Name the blood parasite species.
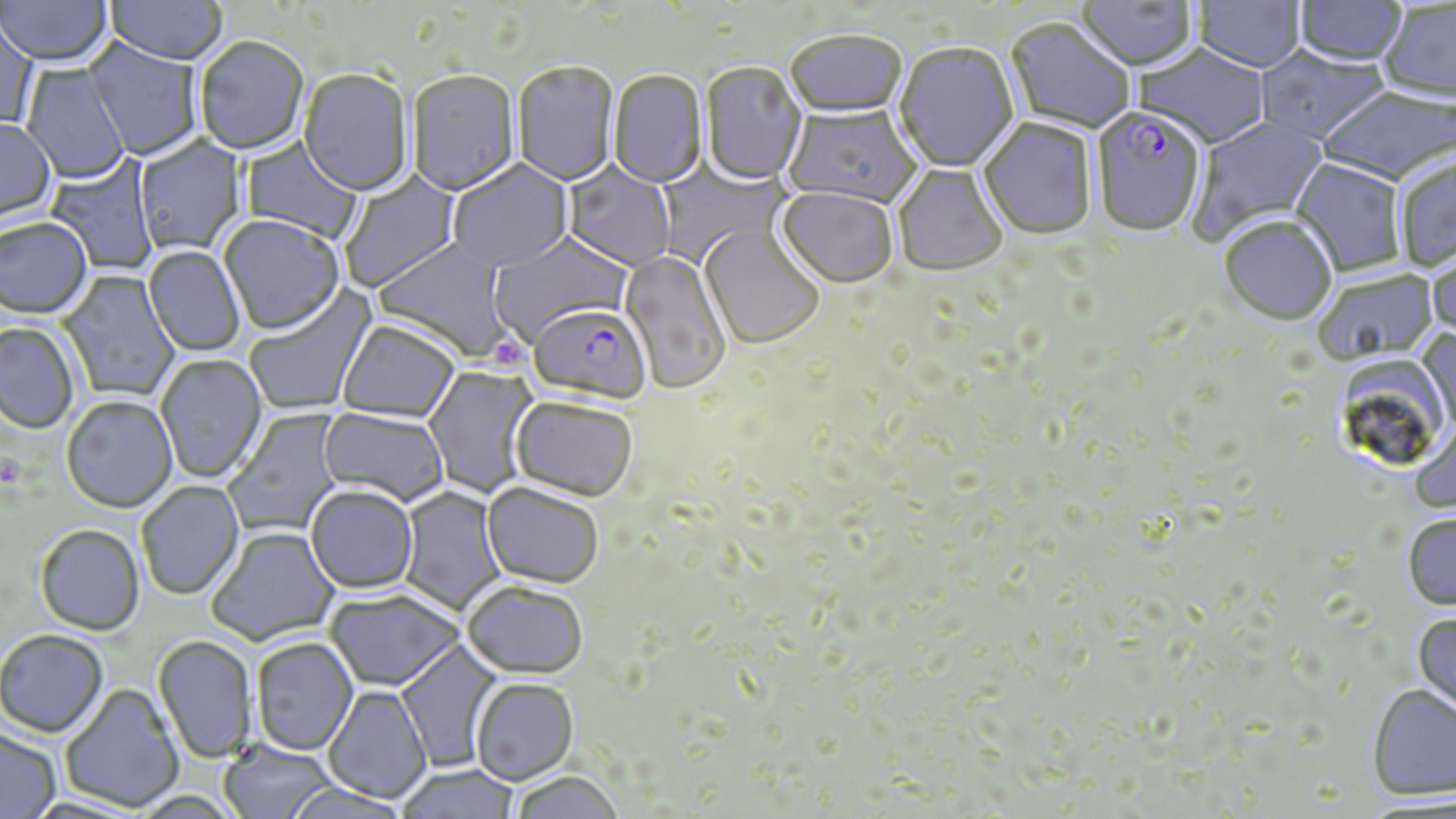

Plasmodium falciparum.

Summary:
  - Coordinate format: approximate bounding boxes as (x1, y1, x2, y2) in pixels
  - Platelet locations: (488, 336, 530, 376)
  - Plasmodium falciparum-infected red blood cell locations: (1089, 109, 1207, 240), (527, 303, 652, 404)
  - Uninfected red blood cell locations: (1, 0, 113, 70), (105, 0, 228, 68), (1075, 0, 1198, 74), (1192, 0, 1306, 75), (1293, 1, 1408, 68), (1378, 2, 1456, 105), (0, 11, 39, 133), (1004, 18, 1135, 136), (785, 33, 907, 121), (83, 37, 205, 162), (195, 39, 309, 157), (894, 43, 1019, 174), (1134, 44, 1271, 151), (1255, 46, 1389, 147), (20, 60, 130, 185), (512, 62, 619, 188), (700, 63, 807, 186), (298, 70, 414, 199), (407, 71, 520, 198), (608, 71, 707, 190), (1317, 86, 1456, 186), (783, 105, 922, 210), (1187, 115, 1329, 245), (0, 119, 57, 227), (978, 119, 1098, 242), (133, 134, 248, 258), (239, 136, 364, 244), (44, 151, 159, 275), (654, 156, 788, 269), (1394, 157, 1456, 273), (1290, 159, 1407, 278), (447, 160, 574, 274), (561, 160, 677, 272), (892, 164, 1008, 277), (338, 168, 463, 295), (776, 188, 898, 289), (218, 217, 345, 337), (1219, 218, 1337, 328), (0, 219, 93, 321), (700, 223, 825, 349), (488, 231, 633, 346), (373, 238, 522, 363), (1427, 243, 1456, 347), (143, 246, 245, 357), (619, 250, 732, 394), (57, 268, 181, 403), (1314, 270, 1439, 367), (244, 283, 378, 416), (336, 320, 461, 422), (0, 323, 78, 436), (1417, 327, 1456, 436), (155, 354, 267, 484), (422, 365, 539, 498), (511, 395, 639, 500), (61, 398, 178, 514), (319, 407, 450, 507), (222, 408, 347, 539), (1410, 417, 1456, 514), (136, 481, 244, 600), (482, 481, 605, 588), (305, 484, 419, 594), (397, 486, 508, 617), (1403, 513, 1456, 610), (35, 526, 145, 637), (205, 526, 340, 648), (461, 579, 588, 678), (324, 588, 466, 691), (1412, 613, 1456, 720), (0, 630, 108, 739), (153, 635, 259, 764), (250, 637, 359, 755), (396, 639, 504, 772), (470, 677, 578, 785), (59, 683, 185, 812), (323, 684, 432, 804), (1366, 684, 1456, 801), (0, 728, 61, 818), (217, 738, 338, 819), (396, 764, 521, 819), (507, 770, 626, 819), (282, 783, 413, 818)
  - Image size: 1456×819 pixels
  - Stain: May-Grünwald-Giemsa
  - Magnification: 1000x
  - Field of view: single
  - Preparation: thin blood smear
  - Modality: optical microscopy